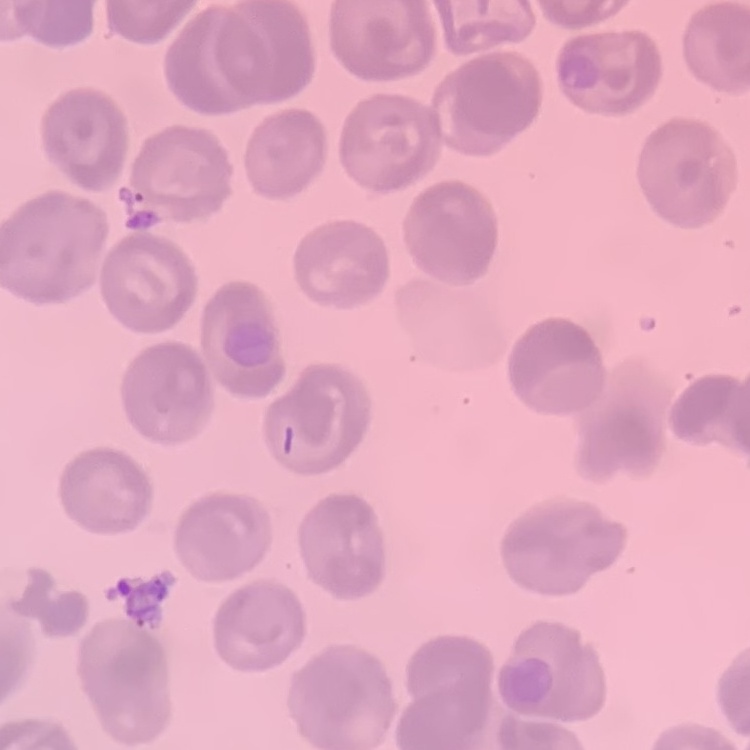
Summary:
  - Erythrocyte morphology: no rouleaux formation
  - Stain: Field's or Giemsa
  - Preparation: thin blood smear
  - Image type: square crop of a larger photomicrograph